Point out each malaria parasite.
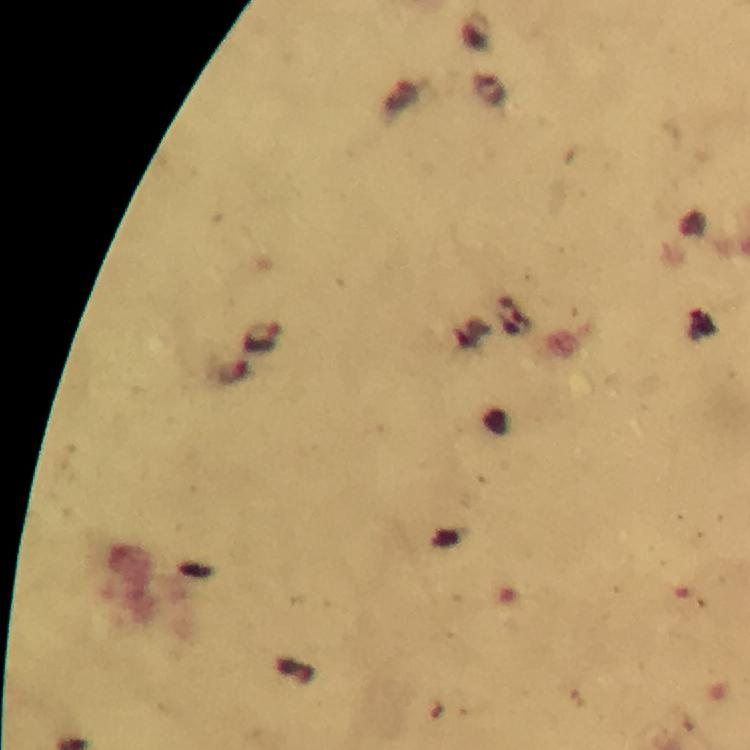

Approximate centers as [x, y] in pixels.
Malaria parasites: [263, 337].

preparation = thick blood film
immersion oil = used
image size = 750×750 pixels
cropped from = a single field of view
stain = Giemsa
capture = smartphone camera through the microscope
magnification = 100x
context = from a malaria diagnostic workup